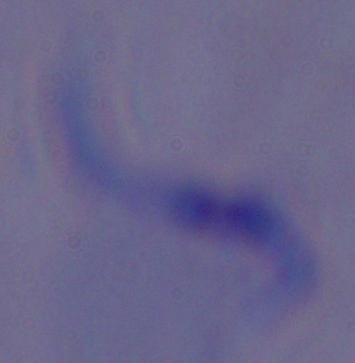
Summary:
  - Modality: micrograph
  - Magnification: 1000x
  - Identification: trypanosome